Assess this cell for malaria.
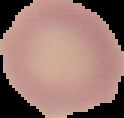
It is uninfected.

The area outside the segmented cell region is set to black. From a thin blood film. Image is 124×118 pixels.